Give the position of every malaria parasite.
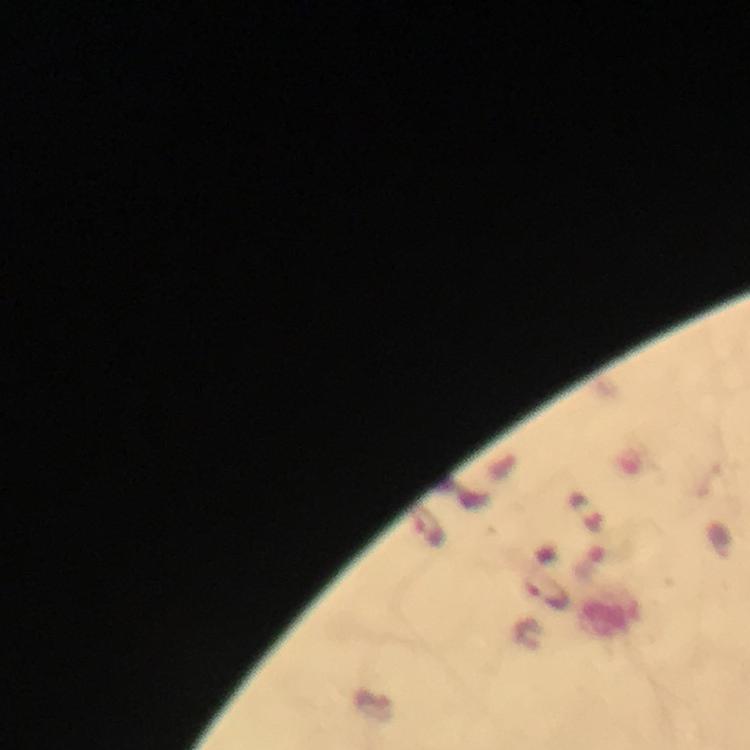

Approximate centers as {x, y} in pixels.
Malaria parasites: {429, 527}, {546, 592}.

Summary:
  - Magnification: 100x
  - Preparation: thick smear
  - Stain: Giemsa
  - Cropped from: one field of view
  - Context: from a diagnostic examination for malaria
  - Image size: 750×750 pixels
  - Capture: smartphone mounted on the microscope
  - Immersion oil: used